Describe the morphology of the red blood cells.
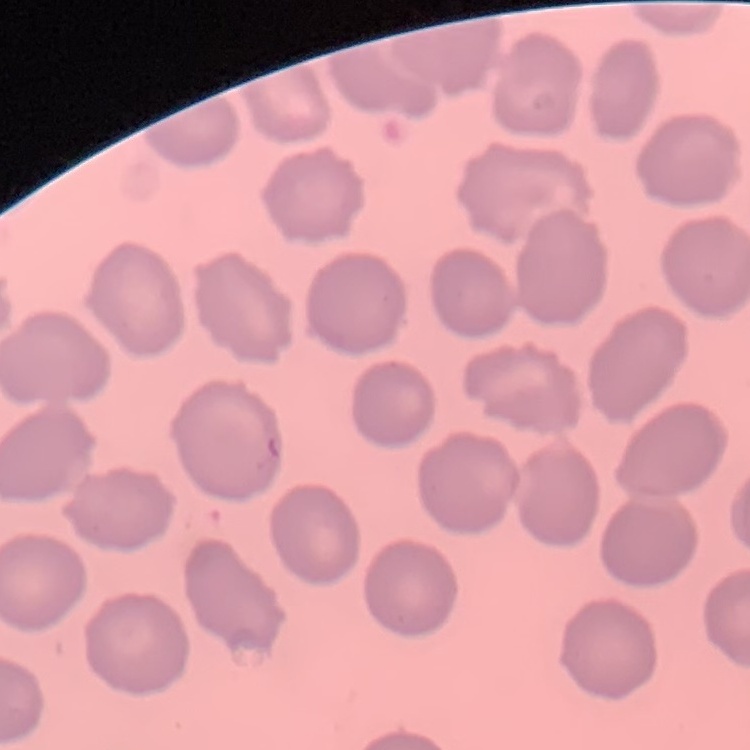
They show no rouleaux formation.

stain = Field's or Giemsa
image type = one tile cut from a larger photomicrograph
preparation = thin peripheral smear